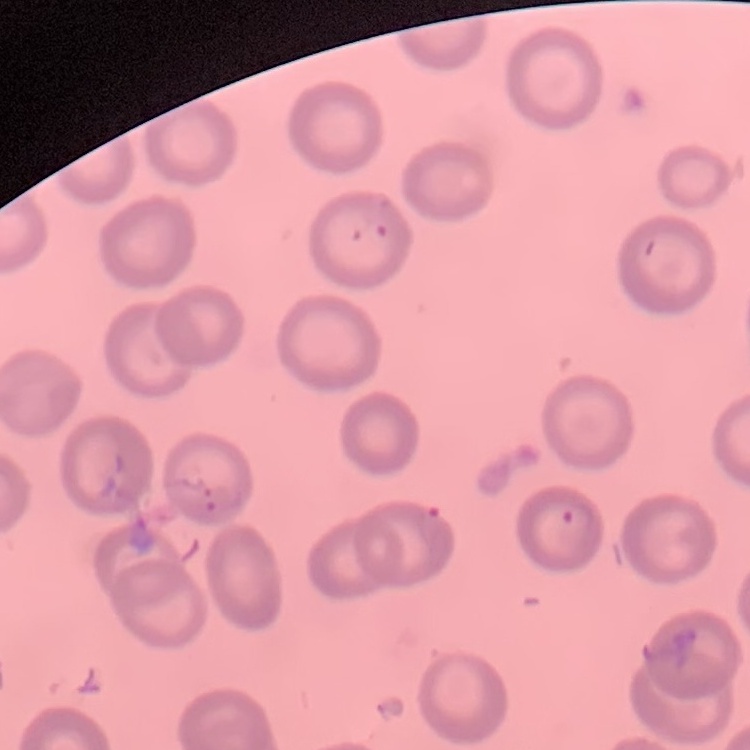

{
  "red_blood_cell_morphology": "no rouleaux formation",
  "stain": "Field's or Giemsa",
  "image_type": "square crop of a larger photomicrograph",
  "preparation": "thin blood smear"
}